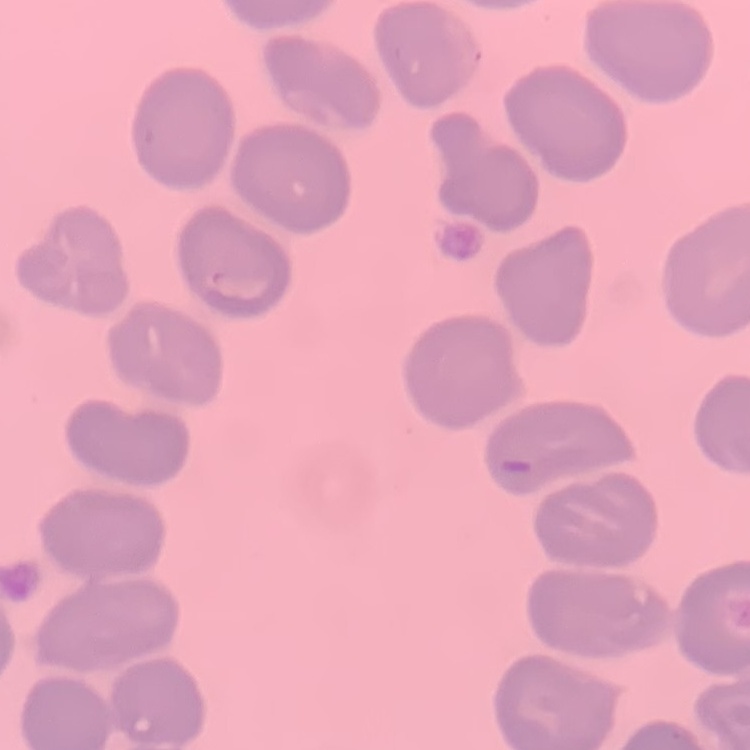
red blood cell morphology = no rouleaux formation
stain = Field's or Giemsa
image type = square crop of a larger photomicrograph
preparation = thin peripheral smear